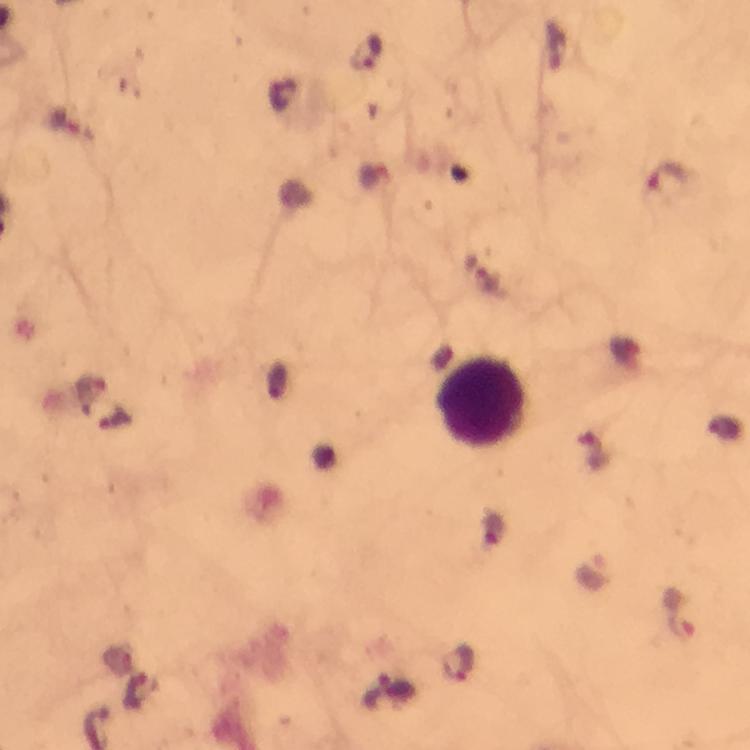
Approximate centers as (x, y) in pixels. Leukocyte locations: (482, 402). Plasmodium parasite locations: (368, 54), (670, 180), (93, 387), (683, 622), (458, 663). Cropped region of a single field of view. Image is 750×750 pixels. Thick smear. Giemsa stain. At 100x magnification. Photographed with a smartphone mounted on the microscope. From a malaria diagnostic workup. Immersion oil applied.